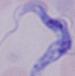
modality: photomicrograph
identification: trypanosome
magnification: 1000x